Give the extent of all Plasmodium falciparum-infected red blood cells.
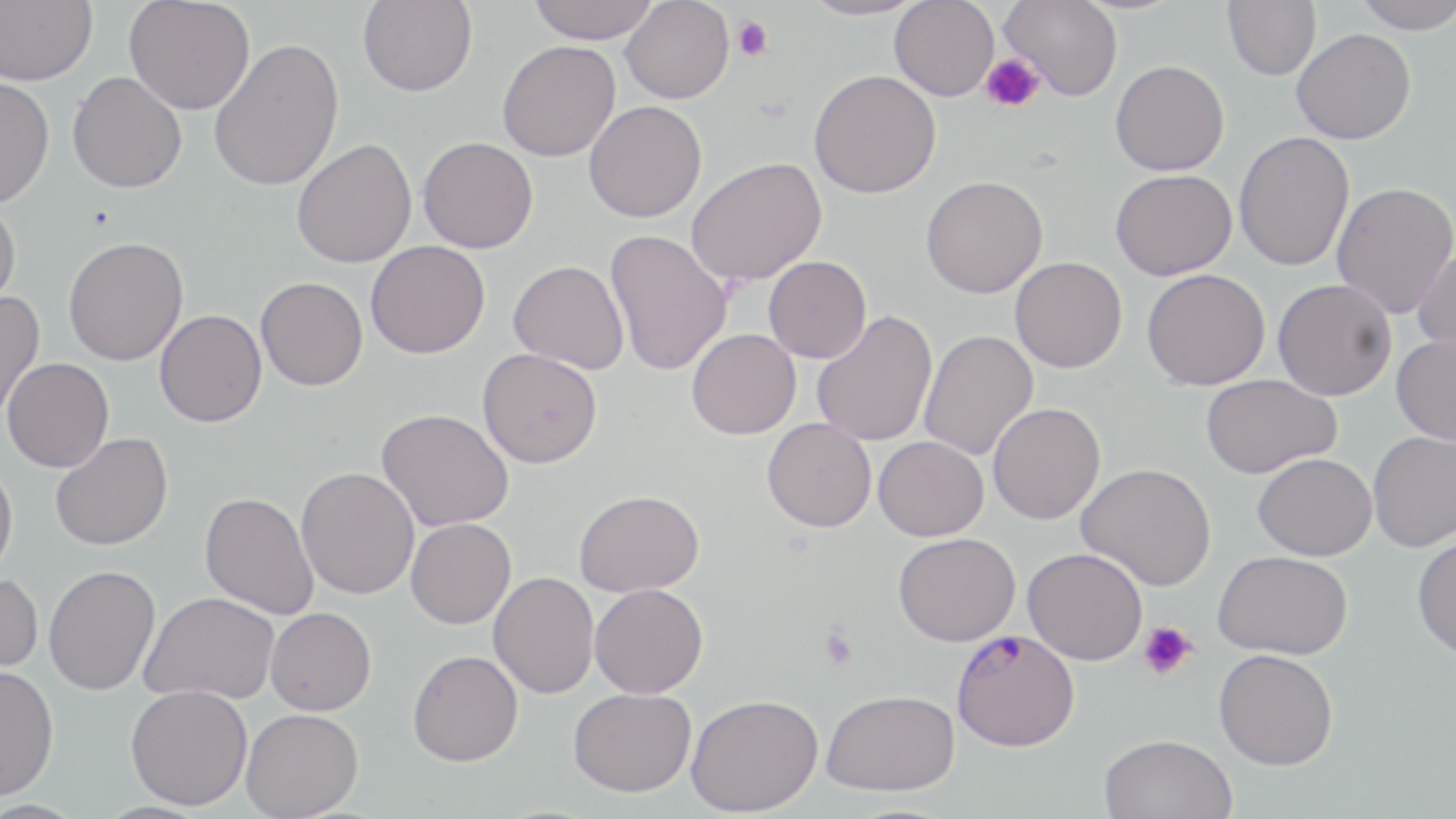
Approximate bounding boxes as (x1,y1)-(x2,y2) corner pairs in pixels.
Plasmodium falciparum-infected red blood cells: (951,628)-(1080,752).

slide-level diagnosis = Plasmodium falciparum
magnification = 1000x
platelet locations = approximate bounding boxes as (x1,y1)-(x2,y2) corner pairs in pixels: (732,16)-(774,61), (980,54)-(1046,113), (1138,621)-(1197,681), (820,626)-(857,670)
uninfected red blood cell locations = approximate bounding boxes as (x1,y1)-(x2,y2) corner pairs in pixels: (0,0)-(97,85), (124,0)-(255,115), (358,0)-(477,96), (525,0)-(659,43), (621,0)-(734,104), (797,0)-(928,20), (999,0)-(1122,101), (1222,0)-(1321,80), (1351,0)-(1456,33), (889,1)-(999,101), (1291,28)-(1415,144), (209,37)-(345,191), (497,40)-(621,162), (1110,60)-(1230,176), (808,69)-(941,198), (67,71)-(187,193), (0,77)-(54,208), (584,100)-(707,223), (1233,131)-(1355,271), (418,137)-(538,253), (291,138)-(416,268), (686,157)-(826,286), (1110,169)-(1237,280), (920,175)-(1047,298), (1331,182)-(1456,319), (0,199)-(20,313), (604,228)-(733,376), (63,236)-(188,366), (365,241)-(490,359), (1412,244)-(1456,356), (763,256)-(872,363), (1010,257)-(1127,373), (508,260)-(629,374), (1141,269)-(1270,390), (256,276)-(368,391), (1272,279)-(1397,401), (0,291)-(45,422), (154,309)-(267,427), (811,310)-(937,447), (686,328)-(801,439), (919,329)-(1038,461), (1391,333)-(1456,445), (477,348)-(602,468), (2,358)-(114,473), (1200,374)-(1341,478), (987,403)-(1105,524), (376,408)-(513,532), (762,418)-(876,532), (1367,431)-(1456,552), (50,432)-(173,551), (873,436)-(989,541), (1252,452)-(1377,560), (0,461)-(18,579), (1075,463)-(1216,591), (295,467)-(419,599), (574,489)-(704,596), (200,491)-(319,619), (406,518)-(516,629), (893,532)-(1020,646), (1412,532)-(1456,661), (1023,547)-(1147,665), (1214,550)-(1352,659), (44,565)-(160,695), (0,572)-(43,676), (488,572)-(599,699), (589,583)-(708,698), (140,592)-(280,705), (265,607)-(376,715), (1213,649)-(1338,770), (408,650)-(523,766), (0,664)-(59,799), (125,684)-(253,810), (567,687)-(696,797), (820,689)-(960,796), (685,693)-(823,816), (241,708)-(364,818), (1099,733)-(1237,819)
preparation = thin blood film
field of view = one of a larger specimen
modality = optical microscopy
image size = 1456×819 pixels
stain = May-Grünwald-Giemsa